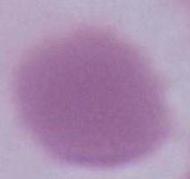
Summary:
  - Magnification: 1000x
  - Identification: red blood cell
  - Modality: micrograph